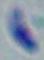 Toxoplasma gondii is shown. Micrograph. Captured at 1000x magnification.